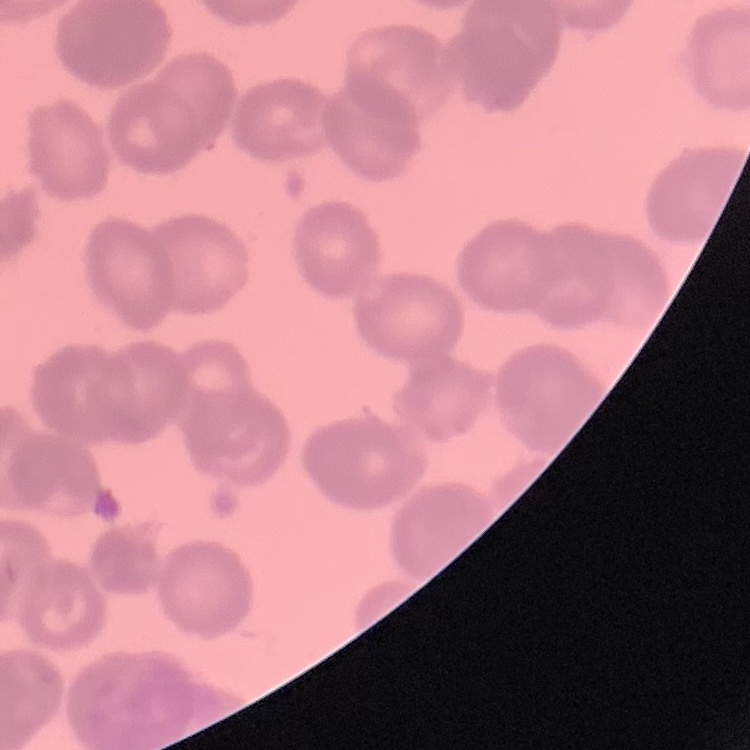
erythrocyte morphology = rouleaux formation
image type = one tile cut from a larger photomicrograph
stain = Field's or Giemsa
preparation = thin peripheral smear